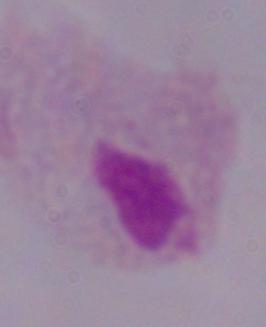

modality = photomicrograph
magnification = 1000x
identification = trichomonad